Report the malaria status of this cell.
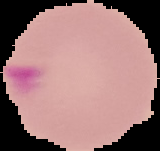
Parasitized.

Image is 160×151 pixels. The area outside the segmented cell region is set to black. From a thin blood smear.